Locate and identify every blood parasite.
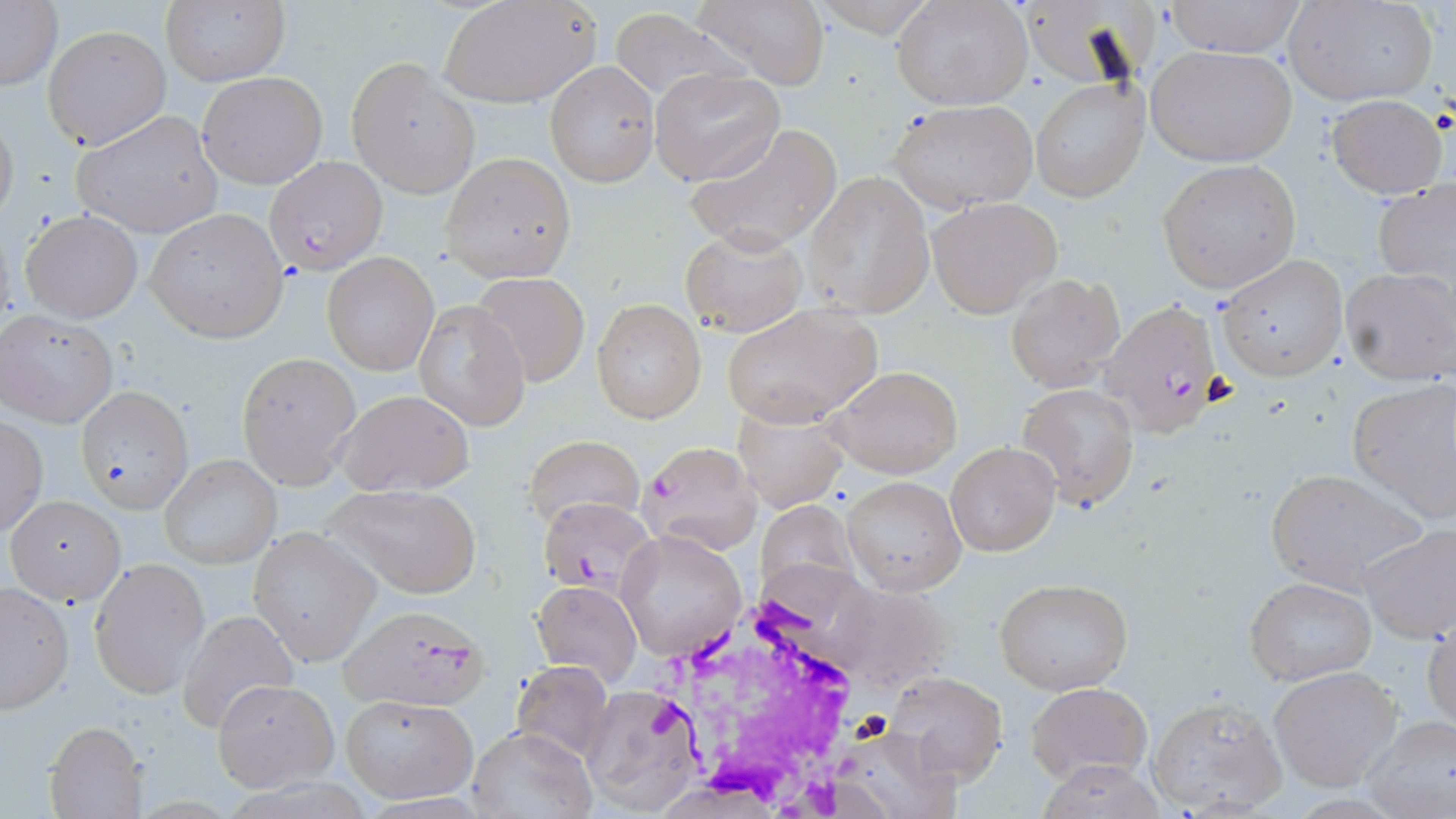
Approximate bounding boxes as named x1/y1/x2/y2 corners in pixels.
Plasmodium falciparum-infected red blood cells: (x1=265, y1=156, x2=387, y2=276), (x1=1102, y1=302, x2=1225, y2=436), (x1=542, y1=502, x2=668, y2=597), (x1=338, y1=605, x2=489, y2=710).
No Plasmodium ovale, Plasmodium malariae, Plasmodium vivax, Babesia divergens, or Trypanosoma brucei observed.

slide-level diagnosis = Plasmodium falciparum
uninfected red blood cell locations = approximate bounding boxes as named x1/y1/x2/y2 corners in pixels: (x1=440, y1=0, x2=602, y2=109), (x1=1286, y1=0, x2=1439, y2=107), (x1=0, y1=1, x2=62, y2=93), (x1=688, y1=1, x2=833, y2=88), (x1=892, y1=1, x2=1033, y2=110), (x1=1161, y1=1, x2=1308, y2=58), (x1=159, y1=2, x2=289, y2=86), (x1=607, y1=8, x2=747, y2=105), (x1=42, y1=24, x2=171, y2=151), (x1=1147, y1=45, x2=1298, y2=168), (x1=345, y1=57, x2=480, y2=198), (x1=544, y1=61, x2=659, y2=187), (x1=651, y1=69, x2=785, y2=184), (x1=197, y1=70, x2=328, y2=190), (x1=1030, y1=79, x2=1148, y2=203), (x1=1327, y1=93, x2=1447, y2=200), (x1=889, y1=99, x2=1039, y2=212), (x1=0, y1=107, x2=20, y2=231), (x1=72, y1=109, x2=224, y2=239), (x1=685, y1=123, x2=842, y2=253), (x1=441, y1=153, x2=575, y2=281), (x1=1158, y1=159, x2=1300, y2=293), (x1=801, y1=171, x2=935, y2=319), (x1=1374, y1=178, x2=1456, y2=291), (x1=927, y1=197, x2=1061, y2=318), (x1=18, y1=208, x2=144, y2=324), (x1=145, y1=209, x2=288, y2=342), (x1=679, y1=225, x2=808, y2=338), (x1=322, y1=253, x2=437, y2=375), (x1=1215, y1=255, x2=1348, y2=381), (x1=1338, y1=266, x2=1455, y2=385), (x1=471, y1=272, x2=590, y2=387), (x1=1006, y1=273, x2=1124, y2=390), (x1=415, y1=299, x2=528, y2=432), (x1=591, y1=299, x2=704, y2=423), (x1=722, y1=303, x2=883, y2=426), (x1=0, y1=308, x2=119, y2=428), (x1=236, y1=353, x2=361, y2=488), (x1=825, y1=364, x2=963, y2=479), (x1=1346, y1=378, x2=1456, y2=522), (x1=1018, y1=383, x2=1140, y2=509), (x1=76, y1=386, x2=193, y2=514), (x1=333, y1=389, x2=475, y2=497), (x1=731, y1=401, x2=847, y2=512), (x1=0, y1=415, x2=47, y2=538), (x1=525, y1=437, x2=644, y2=533), (x1=637, y1=439, x2=761, y2=553), (x1=946, y1=441, x2=1061, y2=557), (x1=159, y1=454, x2=280, y2=570), (x1=1263, y1=468, x2=1429, y2=596), (x1=842, y1=477, x2=965, y2=596), (x1=320, y1=482, x2=481, y2=598), (x1=3, y1=493, x2=126, y2=606), (x1=1357, y1=522, x2=1456, y2=645), (x1=248, y1=526, x2=383, y2=668), (x1=616, y1=528, x2=745, y2=662), (x1=87, y1=557, x2=210, y2=698), (x1=1245, y1=576, x2=1377, y2=687), (x1=994, y1=578, x2=1134, y2=695), (x1=532, y1=579, x2=643, y2=687), (x1=1, y1=582, x2=75, y2=714), (x1=176, y1=609, x2=300, y2=735), (x1=1423, y1=609, x2=1456, y2=735), (x1=510, y1=660, x2=616, y2=761), (x1=1268, y1=665, x2=1406, y2=792), (x1=884, y1=671, x2=1007, y2=784), (x1=210, y1=679, x2=338, y2=792), (x1=579, y1=682, x2=704, y2=816), (x1=1025, y1=683, x2=1151, y2=784), (x1=339, y1=694, x2=478, y2=804), (x1=1147, y1=696, x2=1289, y2=814), (x1=1361, y1=716, x2=1455, y2=819), (x1=44, y1=721, x2=147, y2=818), (x1=468, y1=727, x2=594, y2=818)
modality = optical microscopy
magnification = 1000x
image size = 1456×819 pixels
field of view = one of a larger specimen
preparation = thin blood film
stain = May-Grünwald-Giemsa
white blood cell locations = approximate bounding boxes as named x1/y1/x2/y2 corners in pixels: (x1=640, y1=588, x2=882, y2=811)